Locate every Plasmodium falciparum-infected red blood cell.
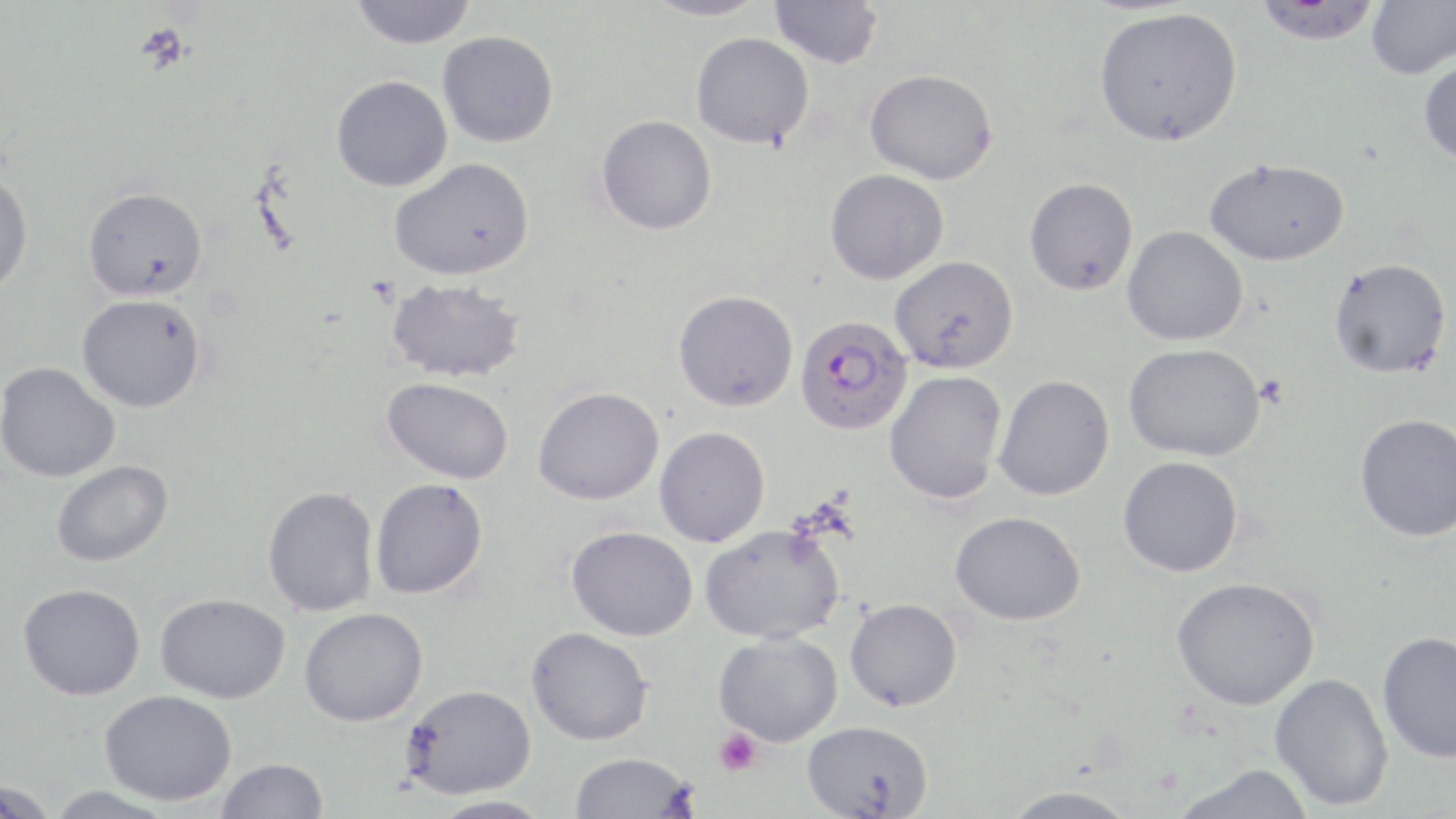
Approximate bounding boxes as named x1/y1/x2/y2 corners in pixels.
Plasmodium falciparum-infected red blood cells: (x1=794, y1=315, x2=913, y2=436).

Summary:
  - Platelet locations: (x1=135, y1=23, x2=192, y2=75), (x1=713, y1=728, x2=762, y2=776)
  - Uninfected red blood cell locations: (x1=349, y1=0, x2=477, y2=49), (x1=641, y1=0, x2=771, y2=21), (x1=769, y1=0, x2=884, y2=69), (x1=1253, y1=0, x2=1382, y2=45), (x1=1366, y1=0, x2=1456, y2=79), (x1=1093, y1=6, x2=1242, y2=147), (x1=437, y1=30, x2=558, y2=148), (x1=691, y1=32, x2=815, y2=149), (x1=1418, y1=55, x2=1456, y2=165), (x1=865, y1=68, x2=998, y2=184), (x1=331, y1=75, x2=453, y2=192), (x1=596, y1=115, x2=717, y2=236), (x1=389, y1=157, x2=534, y2=281), (x1=1204, y1=157, x2=1350, y2=266), (x1=0, y1=169, x2=33, y2=299), (x1=825, y1=169, x2=949, y2=285), (x1=1024, y1=177, x2=1138, y2=296), (x1=83, y1=186, x2=208, y2=302), (x1=1122, y1=226, x2=1249, y2=346), (x1=889, y1=255, x2=1019, y2=374), (x1=1329, y1=258, x2=1452, y2=379), (x1=386, y1=278, x2=526, y2=383), (x1=673, y1=289, x2=799, y2=412), (x1=77, y1=294, x2=206, y2=412), (x1=1124, y1=343, x2=1266, y2=462), (x1=0, y1=362, x2=121, y2=482), (x1=884, y1=369, x2=1008, y2=505), (x1=994, y1=374, x2=1115, y2=500), (x1=382, y1=377, x2=514, y2=484), (x1=533, y1=387, x2=664, y2=505), (x1=1355, y1=413, x2=1456, y2=542), (x1=654, y1=426, x2=770, y2=547), (x1=1118, y1=455, x2=1244, y2=578), (x1=51, y1=460, x2=173, y2=567), (x1=370, y1=478, x2=488, y2=599), (x1=262, y1=486, x2=379, y2=617), (x1=950, y1=511, x2=1086, y2=626), (x1=700, y1=523, x2=844, y2=644), (x1=566, y1=525, x2=698, y2=641), (x1=1171, y1=576, x2=1321, y2=710), (x1=18, y1=583, x2=146, y2=700), (x1=155, y1=593, x2=290, y2=703), (x1=845, y1=598, x2=963, y2=712), (x1=299, y1=607, x2=428, y2=727), (x1=526, y1=626, x2=653, y2=745), (x1=713, y1=631, x2=842, y2=747), (x1=1377, y1=631, x2=1456, y2=763), (x1=1270, y1=673, x2=1394, y2=811), (x1=402, y1=684, x2=536, y2=799), (x1=100, y1=689, x2=237, y2=806), (x1=801, y1=720, x2=934, y2=818), (x1=570, y1=752, x2=697, y2=818), (x1=215, y1=757, x2=328, y2=818), (x1=1169, y1=763, x2=1316, y2=819), (x1=1, y1=777, x2=57, y2=819), (x1=1001, y1=785, x2=1141, y2=819), (x1=46, y1=786, x2=179, y2=818), (x1=426, y1=795, x2=556, y2=819)
  - Slide-level diagnosis: Plasmodium falciparum
  - Modality: optical microscopy
  - Preparation: thin blood smear
  - Image size: 1456×819 pixels
  - Field of view: one of a larger specimen
  - Stain: May-Grünwald-Giemsa
  - Magnification: 1000x